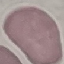

{
  "malaria_status": "uninfected",
  "image_type": "cell patch, automatically extracted from a larger field of view and resized to 64 × 64 pixels",
  "capture": "smartphone through the microscope eyepiece",
  "preparation": "thin smear",
  "stain": "Giemsa"
}